Classify this cell by malaria status.
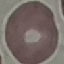

It is uninfected.

Summary:
  - Image type: automatically extracted cell patch, resized to 64 × 64 pixels
  - Capture: smartphone camera at the microscope eyepiece
  - Preparation: thin smear
  - Stain: Giemsa